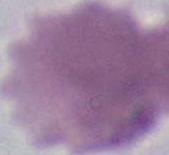
Micrograph. A red blood cell is seen. 1000x magnification.